Classify this cell by malaria status.
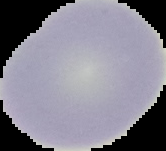
Uninfected.

Image is 166×151 pixels. From a thin blood film. Cell region segmented out of the field of view; the surrounding area is masked to black.